Name the parasite shown.
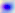
Toxoplasma gondii.

Photomicrograph. Captured at 400x magnification.